Locate every WBC.
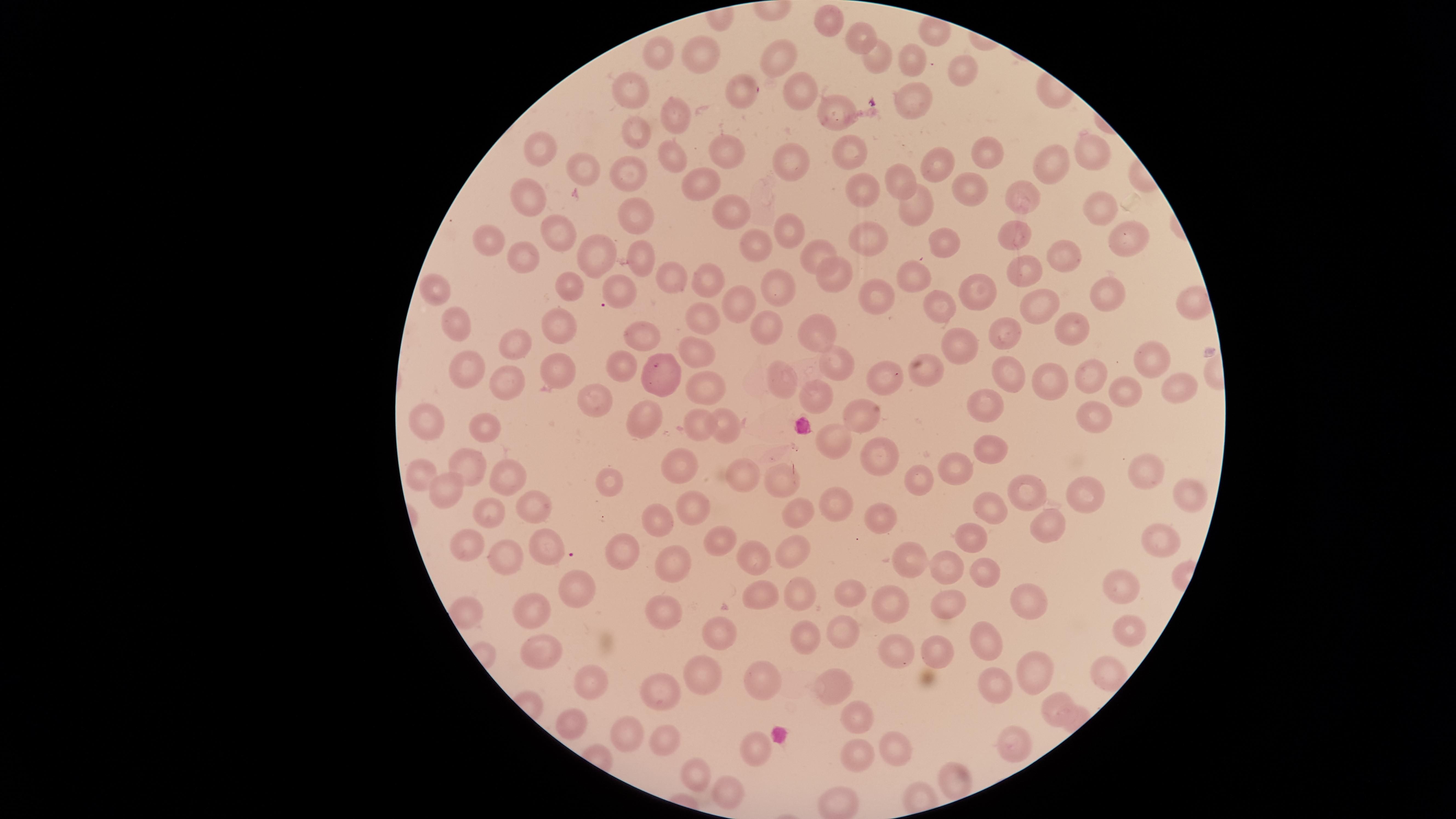
No WBCs identified.

Approximate marker points as (x, y) in pixels.
Summary:
  - Uninfected RBCs: (825, 21), (939, 29), (858, 36), (701, 50), (664, 53), (777, 55), (875, 55), (917, 59), (958, 68), (795, 86), (627, 89), (740, 90), (914, 103), (836, 110), (670, 115), (643, 130), (537, 147), (851, 147), (984, 151), (1089, 152), (733, 153), (675, 155), (791, 159), (1051, 164), (945, 165), (584, 168), (707, 175), (639, 176), (897, 181), (858, 186), (973, 187), (534, 196), (1025, 199), (920, 202), (730, 203), (1096, 204), (637, 210), (788, 224), (555, 230), (494, 235), (1019, 235), (865, 237), (1119, 238), (938, 239), (761, 241), (814, 250), (590, 251), (522, 253), (1067, 257), (642, 259), (831, 271), (1027, 271), (918, 272), (666, 276), (698, 278), (434, 281), (782, 282), (567, 285), (979, 286), (624, 287), (1108, 291), (878, 292), (737, 299), (1042, 300), (936, 303), (455, 312), (705, 316), (557, 319), (760, 321), (1002, 328), (1070, 329), (816, 334), (639, 337), (520, 343), (962, 343), (702, 351), (1148, 357), (466, 358), (834, 358), (1008, 365), (614, 366), (552, 368), (927, 368), (1094, 377), (512, 378), (662, 379), (780, 380), (878, 381), (1048, 383), (706, 385), (1177, 385), (1133, 388), (820, 394), (598, 401), (992, 405), (858, 409), (1095, 412), (420, 420), (653, 420), (485, 421), (703, 421), (729, 422), (832, 438), (875, 447), (990, 449), (959, 457), (473, 462), (679, 462), (419, 470), (510, 471), (744, 471), (1148, 471), (781, 475), (611, 477), (923, 478), (449, 483), (1023, 488), (1093, 491), (1191, 493), (523, 502), (834, 504), (800, 506), (689, 508), (990, 508), (490, 514), (882, 517), (653, 520), (1051, 524), (719, 537), (467, 538), (1163, 541), (973, 542), (545, 545), (911, 549), (781, 551), (624, 554), (504, 555), (761, 561), (675, 563), (950, 567), (982, 571), (1127, 578), (571, 584), (800, 591), (853, 592), (1024, 594), (757, 596), (893, 598), (946, 598), (658, 608), (538, 610), (465, 614), (718, 627), (1133, 629), (840, 632), (990, 634), (803, 637), (941, 649), (900, 651), (538, 655), (1033, 664), (704, 670), (1102, 673), (833, 682), (996, 682), (590, 683), (761, 683), (663, 684), (1054, 703), (849, 712), (568, 721), (624, 732), (665, 738), (1011, 740), (758, 748), (861, 751), (903, 753), (694, 770), (952, 774), (726, 795), (840, 796)
  - Image size: 1456×819 pixels
  - Capture: smartphone photograph through the microscope eyepiece
  - Field of view: single
  - Stain: Giemsa
  - Visible region: circular
  - Preparation: thin blood smear
  - Presence: no malaria parasites detected